Evaluate for Plasmodium parasites.
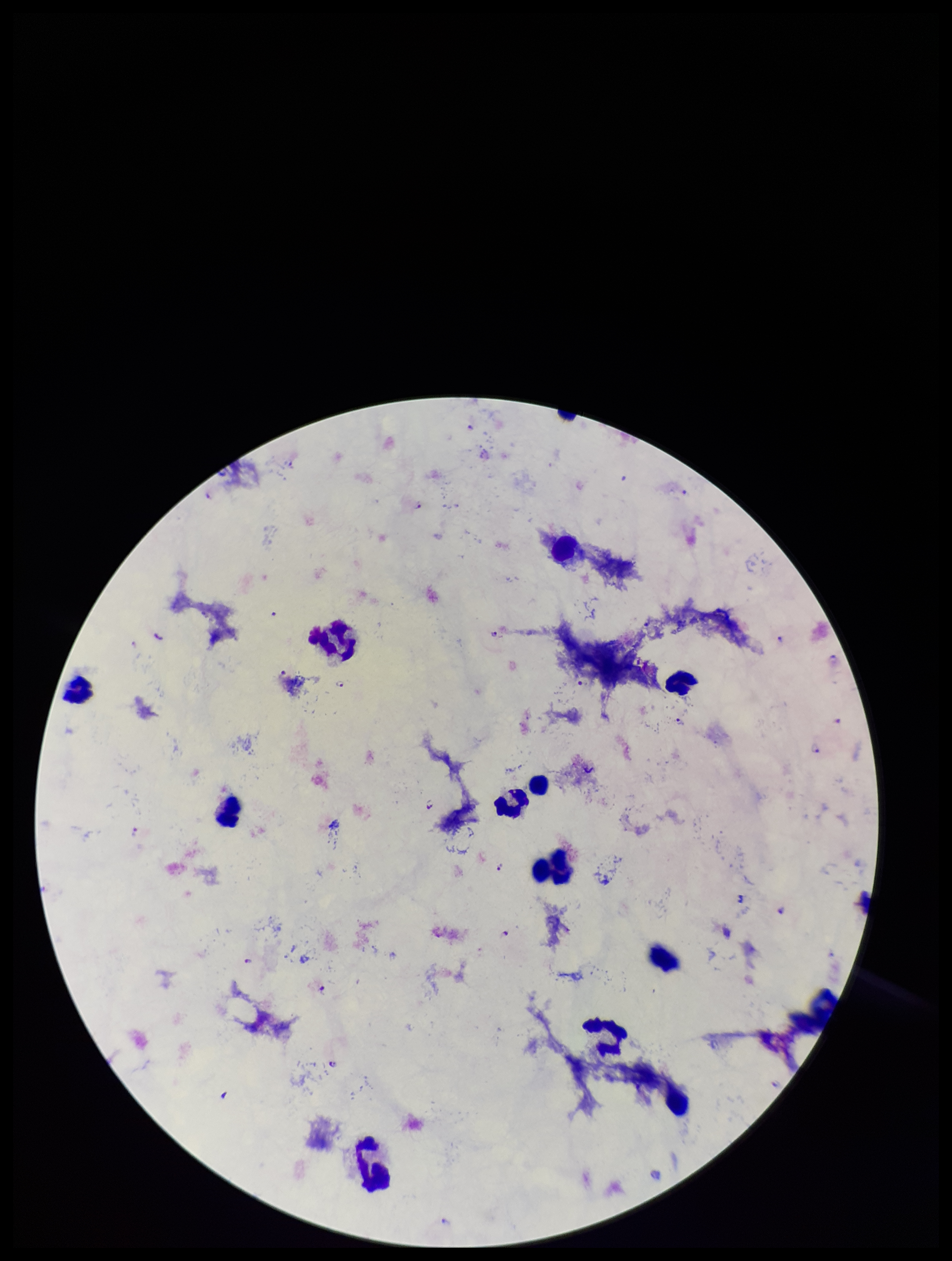

Seen.

Parasite count: 20. Stained with Giemsa. Species reported for this patient: Plasmodium falciparum. Patient malaria status: infected. Single field of view. Preparation: thick blood smear. Leukocyte count: 12. Image is 952×1261 pixels. Photographed through the microscope eyepiece with a smartphone camera.